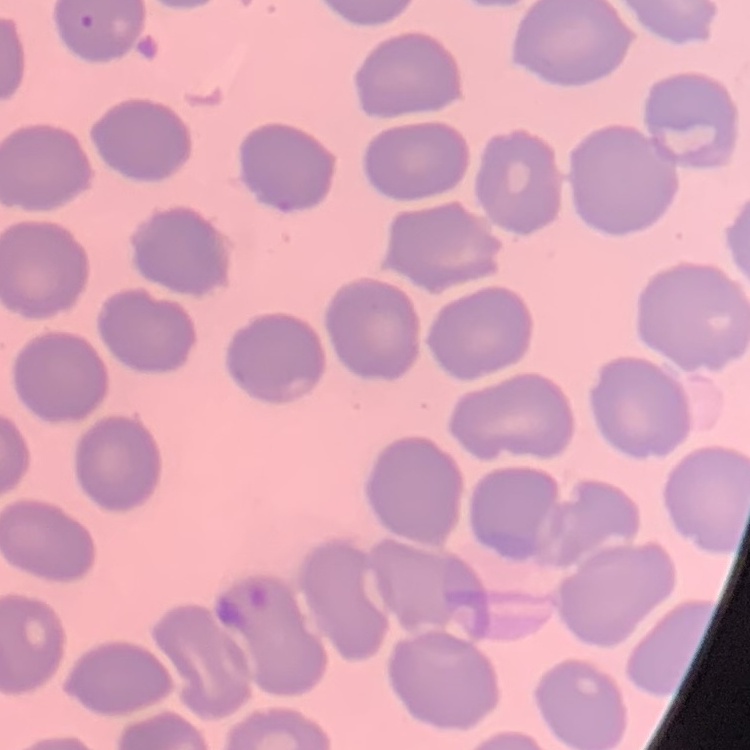 The red blood cells show no rouleaux formation. Thin peripheral smear. One tile cut from a larger photomicrograph. Field's or Giemsa stain.